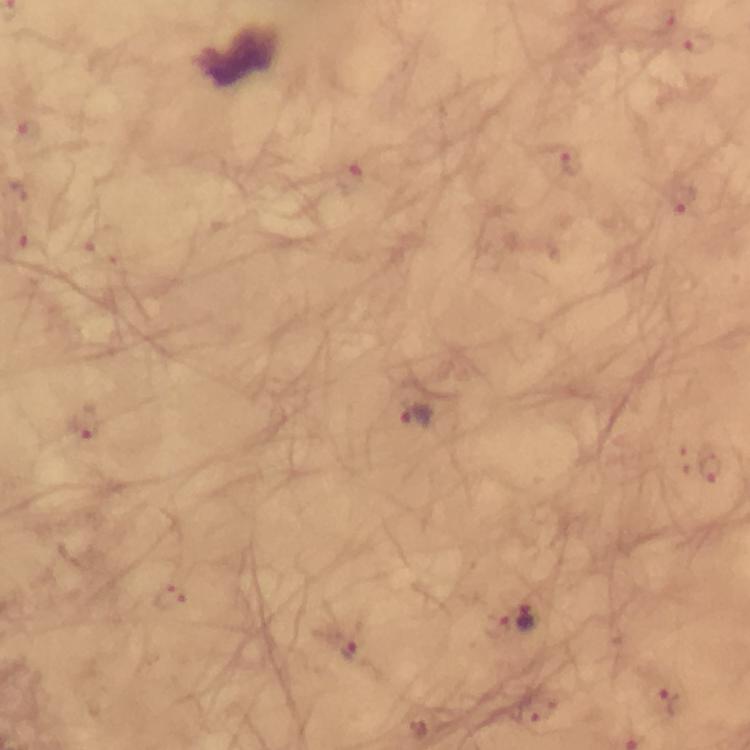

Approximate centers as {x, y} in pixels.
Summary:
  - Plasmodium parasite locations: {663, 21}, {699, 41}, {26, 132}, {570, 161}, {353, 177}, {681, 199}, {105, 248}, {416, 417}, {81, 426}, {682, 463}, {712, 469}, {172, 598}, {526, 616}, {499, 625}, {347, 652}, {666, 702}, {540, 710}
  - Capture: smartphone mounted on the microscope
  - Magnification: 100x
  - Stain: Giemsa
  - Cropped from: a single field of view
  - Context: from a malaria diagnostic workup
  - Image size: 750×750 pixels
  - Preparation: thick blood film
  - Immersion oil: applied